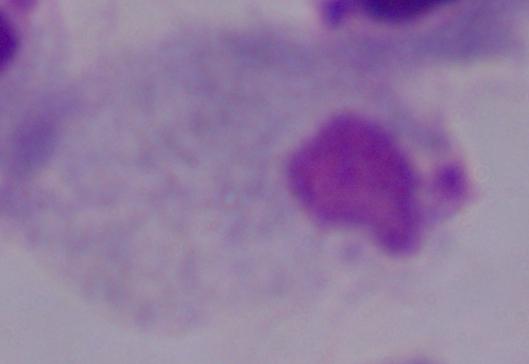

Summary:
  - Magnification: 1000x
  - Identification: trichomonad
  - Modality: photomicrograph